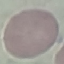

Malaria status: uninfected. Giemsa-stained preparation. Thin blood film. Photographed with a smartphone camera at the microscope eyepiece. Automatically extracted cell patch, resized to 64 × 64 pixels.